Classify the preparation.
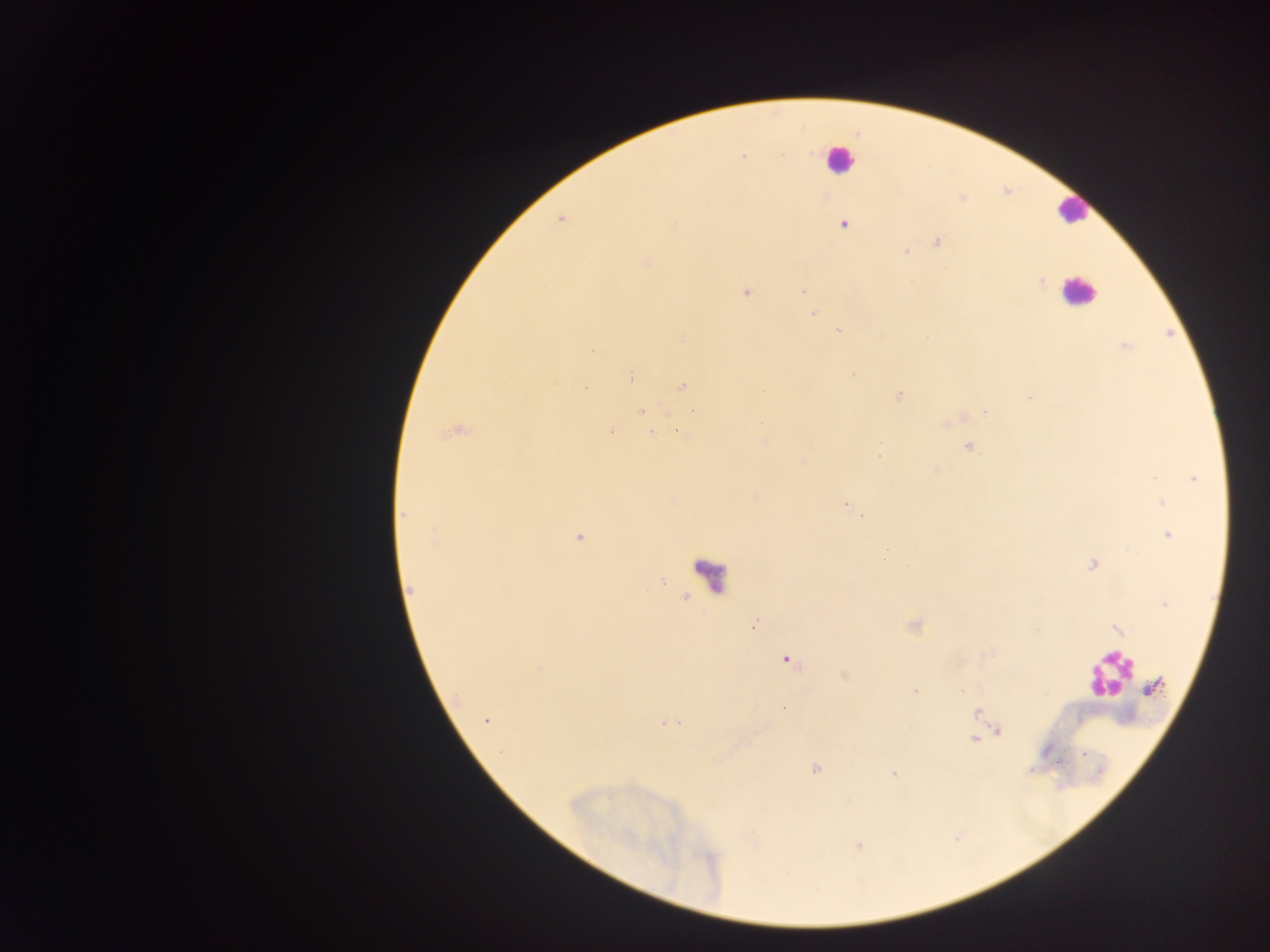

Thick blood film.

Approximate centers as [x, y] in pixels. Leukocyte locations: [838, 159], [1072, 210], [1079, 291], [711, 577], [1108, 676]. Malaria parasite locations: [743, 157], [962, 198], [560, 220], [675, 224], [844, 224], [937, 241], [905, 251], [645, 262], [1042, 280], [803, 291], [746, 292], [813, 313], [839, 331], [1125, 347], [593, 349], [853, 374], [630, 376], [682, 386], [585, 387], [899, 396], [1030, 397], [641, 412], [985, 412], [454, 432], [611, 432], [652, 433], [680, 433], [968, 446], [879, 456], [803, 461], [936, 470], [1194, 479], [1162, 502], [845, 504], [404, 514], [860, 516], [1169, 535], [579, 537], [433, 541], [908, 565], [1092, 566], [410, 589], [1164, 604], [754, 625], [1117, 628], [788, 660], [1154, 687], [962, 690], [915, 691], [784, 708], [977, 713], [486, 720], [668, 723], [999, 732], [974, 739], [815, 770], [893, 773]. Collected in Ghana. Mobile-phone photograph taken through the microscope. One field of view. Image is 1270×952 pixels.